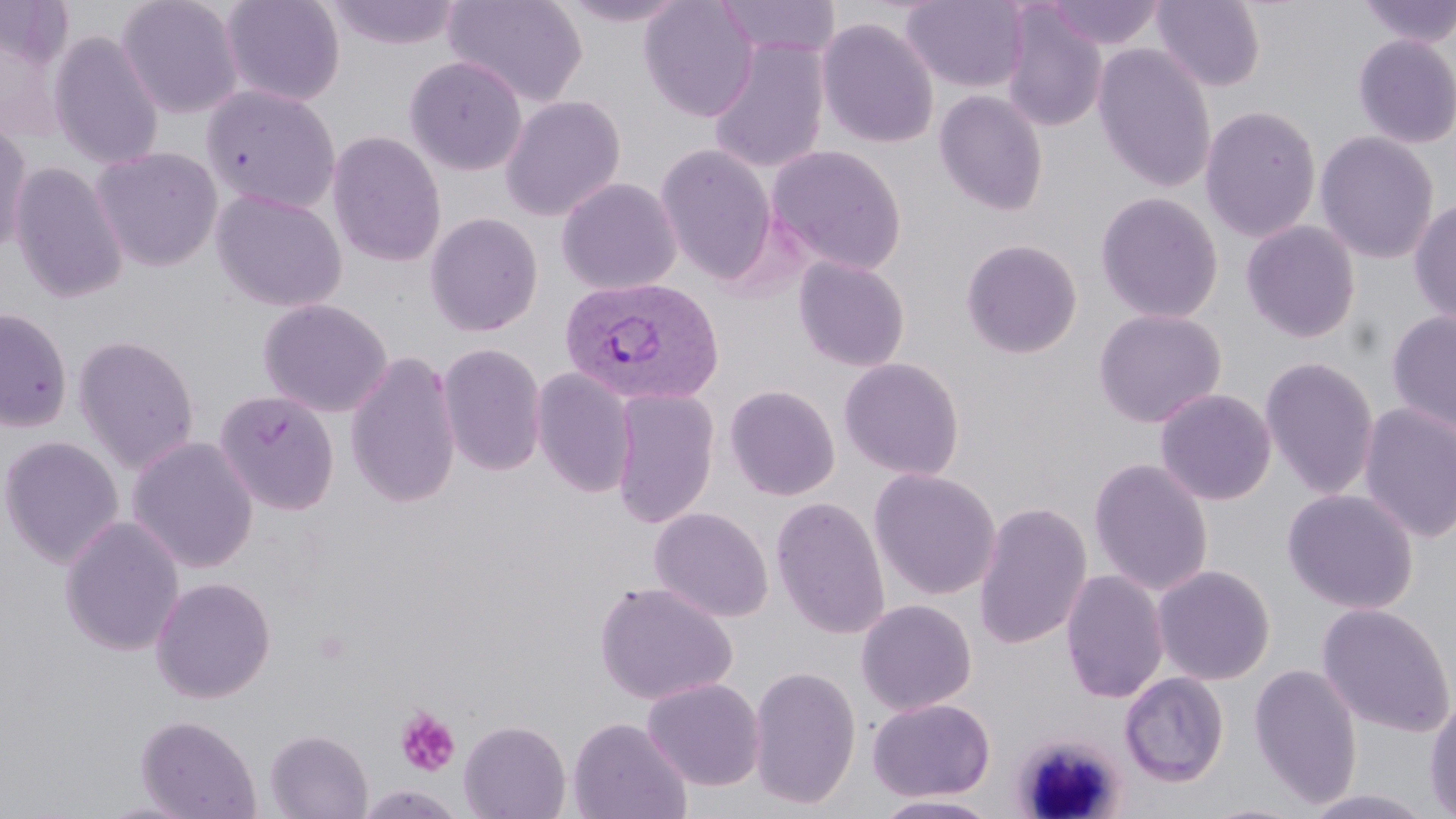

{
  "slide_level_diagnosis": "Plasmodium vivax",
  "uninfected_red_blood_cell_locations": "approximate bounding boxes as [x1, y1, x2, y2] in pixels: [115, 0, 244, 119], [220, 0, 346, 107], [443, 0, 588, 107], [554, 0, 694, 27], [639, 0, 759, 122], [714, 0, 841, 59], [901, 0, 1029, 94], [1046, 0, 1166, 50], [1151, 0, 1267, 91], [1355, 0, 1456, 48], [324, 1, 462, 50], [1000, 5, 1108, 132], [816, 17, 939, 149], [48, 31, 164, 171], [1352, 33, 1456, 149], [707, 38, 830, 174], [1092, 43, 1217, 193], [404, 55, 528, 176], [201, 85, 340, 213], [933, 89, 1048, 216], [500, 94, 627, 221], [1199, 105, 1322, 243], [0, 117, 33, 261], [326, 130, 447, 268], [1315, 130, 1440, 264], [654, 143, 778, 284], [766, 145, 908, 274], [90, 147, 223, 272], [9, 161, 129, 304], [556, 177, 682, 296], [210, 188, 347, 312], [1095, 191, 1224, 324], [1408, 197, 1456, 328], [425, 212, 543, 337], [1240, 220, 1361, 343], [960, 238, 1083, 358], [793, 257, 911, 372], [258, 298, 393, 418], [0, 307, 73, 432], [1093, 308, 1227, 428], [1386, 309, 1456, 436], [72, 334, 200, 473], [437, 342, 547, 477], [345, 349, 462, 510], [1259, 356, 1380, 500], [839, 357, 965, 481], [531, 367, 636, 498], [723, 379, 966, 493], [724, 384, 841, 501], [610, 387, 720, 529], [1154, 387, 1277, 505], [214, 389, 339, 515], [1358, 402, 1456, 544], [0, 435, 124, 568], [126, 435, 260, 574], [1088, 458, 1213, 596], [869, 468, 1001, 601], [1281, 488, 1418, 614], [770, 495, 891, 639], [973, 500, 1093, 651], [648, 506, 774, 623], [58, 515, 186, 657], [1152, 564, 1275, 685], [1060, 570, 1169, 704], [150, 576, 276, 703], [594, 581, 738, 706], [855, 599, 977, 716], [1316, 603, 1455, 737], [1247, 663, 1363, 809], [748, 665, 861, 809], [1119, 671, 1230, 787], [642, 677, 765, 791], [1424, 696, 1456, 819], [867, 698, 995, 802], [134, 714, 261, 819], [567, 716, 692, 819], [458, 719, 571, 819], [265, 729, 373, 818], [1299, 789, 1440, 818], [870, 794, 1004, 818], [1194, 801, 1314, 819]",
  "plasmodium_vivax_infected_red_blood_cell_locations": "approximate bounding boxes as [x1, y1, x2, y2] in pixels: [559, 276, 726, 407]",
  "magnification": "1000x",
  "preparation": "thin blood smear",
  "stain": "May-Grünwald-Giemsa",
  "modality": "light microscopy",
  "field_of_view": "one of a larger specimen",
  "image_size": "1456×819 pixels",
  "platelet_locations": "approximate bounding boxes as [x1, y1, x2, y2] in pixels: [394, 706, 461, 776]"
}